Assess this cell for malaria.
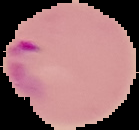

Parasitized.

Summary:
  - Image type: segmented cell region on a black background
  - Image size: 139×130 pixels
  - Preparation: thin blood smear